State which parasite is depicted.
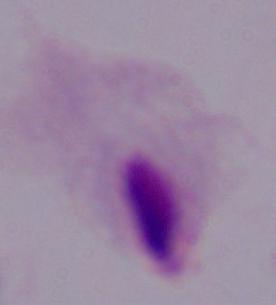
A trichomonad.

Summary:
  - Modality: micrograph
  - Magnification: 1000x